Assess this cell for malaria.
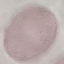
It is uninfected.

{
  "preparation": "thin blood film",
  "capture": "smartphone camera at the microscope eyepiece",
  "image_type": "automatically extracted cell patch, resized to 64 × 64 pixels",
  "stain": "Giemsa"
}